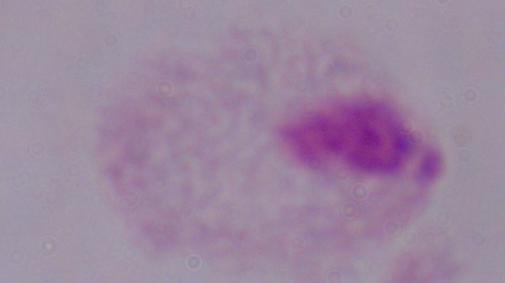
magnification = 1000x
identification = trichomonad
modality = photomicrograph